Report the malaria status of this cell.
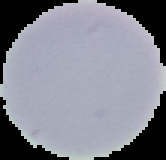

It is uninfected.

image_type: segmented cell region on a black background
preparation: thin blood film
image_size: 166×160 pixels